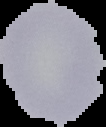

Summary:
  - Preparation: thin blood smear
  - Image size: 106×127 pixels
  - Malaria status: uninfected
  - Image type: segmented cell region on a black background